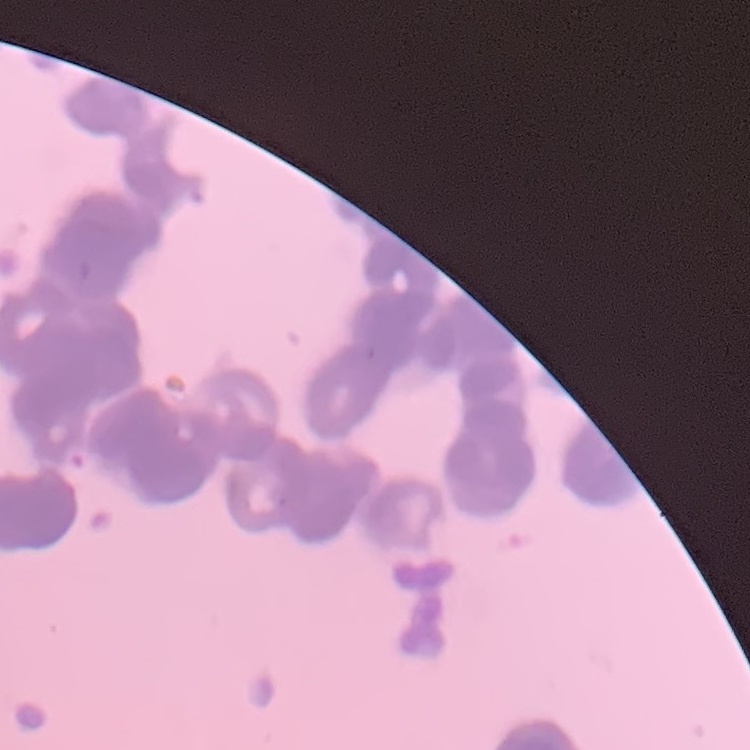

Summary:
  - Red blood cell morphology: rouleaux formation
  - Image type: one tile cut from a larger photomicrograph
  - Preparation: thin blood film
  - Stain: Field's or Giemsa